Assess this cell for malaria.
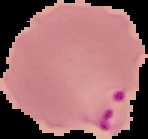

Parasitized.

Cell region segmented out of the field of view; the surrounding area is masked to black. Image is 148×139 pixels. From a thin blood smear.